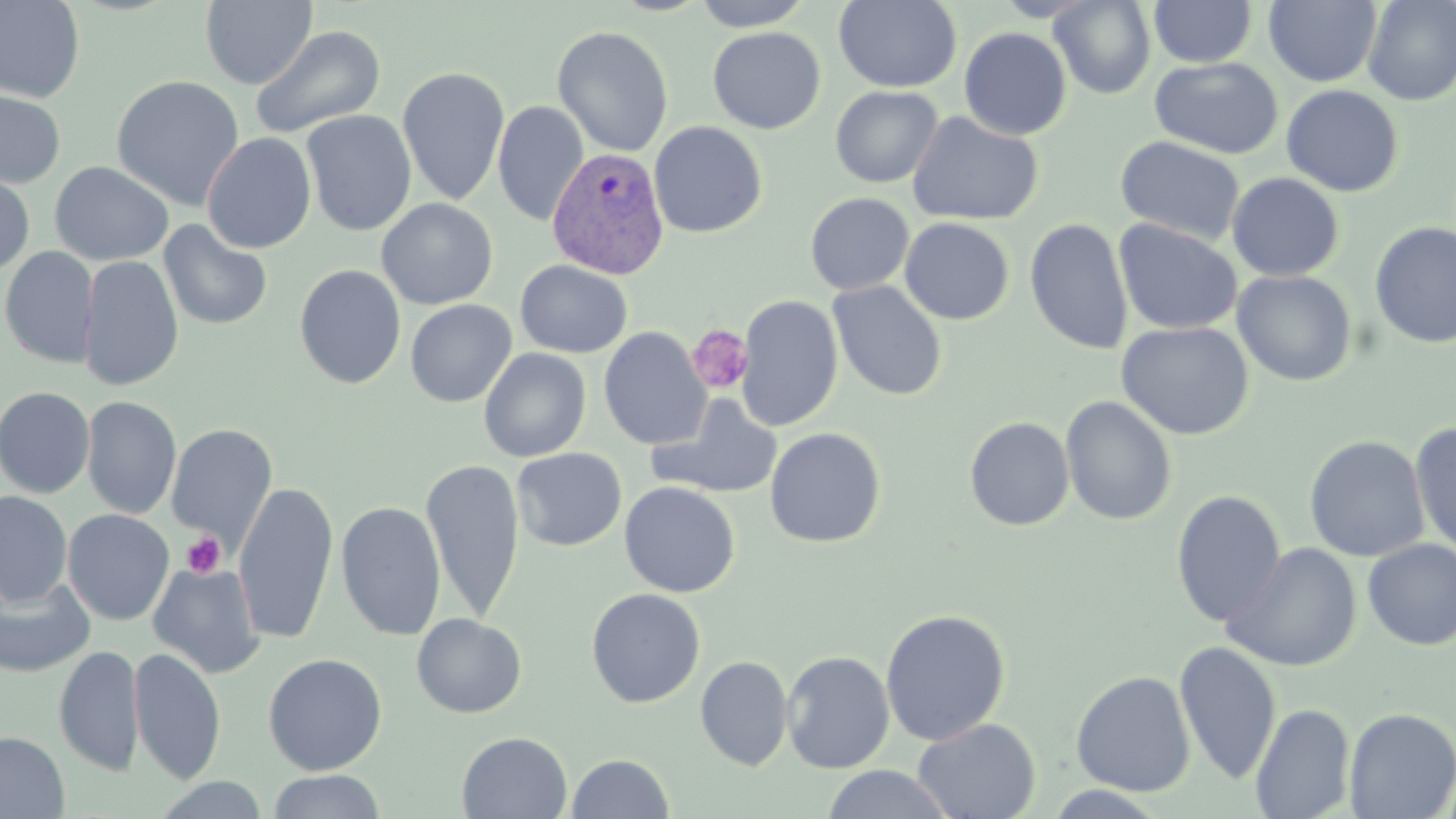

Approximate bounding boxes as (x1, y1, x2, y2) in pixels. Platelet locations: (686, 324, 754, 395), (181, 532, 226, 578). Plasmodium vivax-infected red blood cell locations: (547, 147, 670, 279). Uninfected red blood cell locations: (199, 0, 317, 89), (691, 0, 815, 31), (833, 0, 962, 92), (1048, 0, 1156, 99), (1149, 0, 1258, 68), (1264, 0, 1383, 87), (1361, 0, 1456, 107), (0, 1, 85, 103), (251, 25, 386, 140), (552, 25, 673, 157), (707, 26, 826, 134), (959, 27, 1072, 140), (1149, 56, 1284, 159), (396, 67, 510, 205), (110, 74, 246, 211), (1280, 84, 1404, 197), (0, 86, 66, 189), (830, 86, 943, 188), (492, 100, 589, 227), (300, 110, 417, 236), (907, 111, 1044, 227), (648, 121, 767, 238), (201, 132, 317, 253), (1115, 136, 1246, 246), (49, 161, 174, 266), (0, 169, 35, 278), (1227, 172, 1345, 281), (805, 193, 914, 295), (376, 198, 498, 309), (900, 217, 1014, 325), (1024, 217, 1133, 355), (1113, 219, 1243, 335), (158, 220, 273, 330), (1369, 221, 1456, 349), (1, 246, 98, 367), (79, 254, 184, 392), (515, 260, 633, 358), (294, 263, 406, 389), (1231, 270, 1357, 387), (828, 279, 947, 401), (736, 294, 843, 431), (405, 299, 517, 407), (1115, 321, 1254, 440), (598, 326, 711, 451), (478, 348, 591, 462), (0, 386, 96, 499), (648, 392, 784, 499), (1060, 395, 1177, 526), (81, 396, 182, 520), (964, 416, 1074, 531), (1409, 422, 1456, 559), (166, 423, 278, 550), (765, 428, 886, 548), (1303, 435, 1430, 563), (512, 448, 626, 551), (421, 458, 525, 624), (619, 481, 739, 597), (233, 482, 339, 644), (1171, 490, 1287, 628), (0, 491, 72, 607), (336, 501, 446, 641), (62, 509, 174, 626), (1362, 538, 1456, 650), (1221, 542, 1362, 672), (147, 562, 266, 679), (0, 576, 95, 677), (586, 588, 706, 708), (880, 609, 1011, 746), (411, 613, 527, 718), (1174, 641, 1281, 784), (54, 645, 144, 777), (129, 647, 226, 785), (781, 650, 895, 774), (263, 653, 387, 775), (695, 656, 793, 772), (1071, 670, 1196, 797), (1251, 703, 1356, 819), (1343, 708, 1456, 818), (911, 716, 1041, 819), (0, 731, 69, 819), (457, 731, 573, 818), (566, 753, 674, 818), (820, 765, 956, 819), (268, 770, 386, 819), (154, 775, 271, 818), (1043, 785, 1169, 818). Slide-level diagnosis: Plasmodium vivax. Light microscopy. Image is 1456×819 pixels. May-Grünwald-Giemsa-stained preparation. Thin blood smear. One field of a larger specimen. 1000x magnification.